Mark where platelets are.
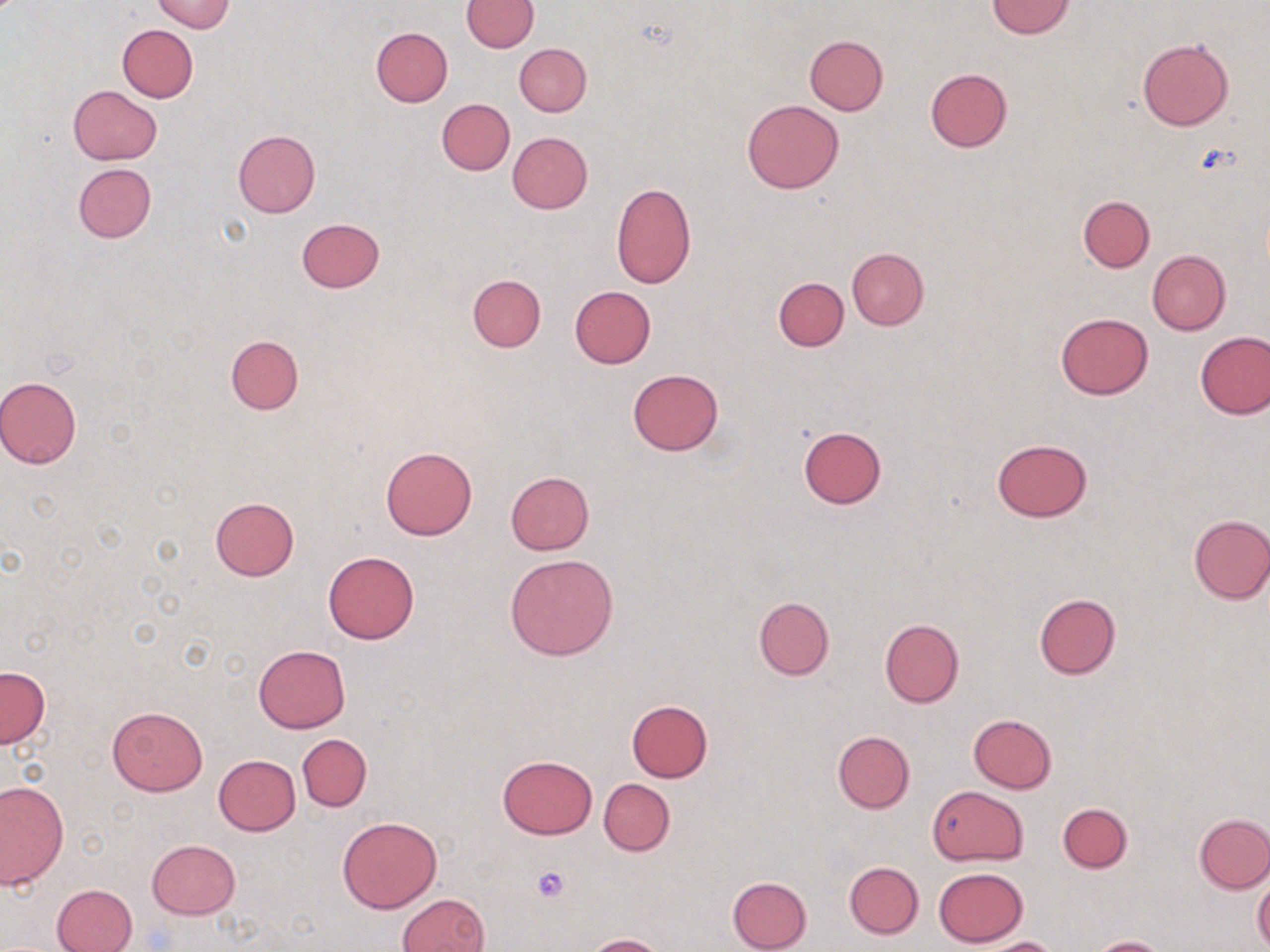

Approximate bounding boxes as named x1/y1/x2/y2 corners in pixels.
Platelets: (x1=532, y1=866, x2=569, y2=902).

Uninfected red blood cell locations: (x1=149, y1=0, x2=235, y2=33), (x1=462, y1=0, x2=537, y2=52), (x1=986, y1=1, x2=1076, y2=39), (x1=117, y1=24, x2=197, y2=102), (x1=370, y1=27, x2=452, y2=107), (x1=803, y1=35, x2=888, y2=115), (x1=1137, y1=38, x2=1234, y2=131), (x1=514, y1=42, x2=591, y2=116), (x1=925, y1=68, x2=1013, y2=152), (x1=69, y1=85, x2=162, y2=164), (x1=436, y1=99, x2=515, y2=175), (x1=741, y1=99, x2=844, y2=194), (x1=232, y1=129, x2=319, y2=218), (x1=507, y1=132, x2=593, y2=214), (x1=73, y1=163, x2=156, y2=243), (x1=611, y1=180, x2=696, y2=289), (x1=1078, y1=195, x2=1155, y2=272), (x1=296, y1=218, x2=385, y2=292), (x1=846, y1=248, x2=928, y2=330), (x1=1148, y1=250, x2=1230, y2=335), (x1=467, y1=274, x2=545, y2=351), (x1=774, y1=277, x2=849, y2=350), (x1=569, y1=286, x2=656, y2=368), (x1=1055, y1=311, x2=1154, y2=400), (x1=1195, y1=331, x2=1269, y2=419), (x1=225, y1=334, x2=304, y2=415), (x1=627, y1=368, x2=724, y2=455), (x1=0, y1=375, x2=81, y2=469), (x1=796, y1=427, x2=887, y2=509), (x1=991, y1=438, x2=1094, y2=523), (x1=381, y1=446, x2=477, y2=540), (x1=506, y1=471, x2=594, y2=554), (x1=210, y1=497, x2=300, y2=580), (x1=1186, y1=514, x2=1270, y2=604), (x1=323, y1=551, x2=418, y2=644), (x1=505, y1=553, x2=618, y2=661), (x1=1033, y1=593, x2=1121, y2=680), (x1=754, y1=596, x2=835, y2=681), (x1=880, y1=619, x2=964, y2=708), (x1=253, y1=645, x2=351, y2=733), (x1=0, y1=666, x2=50, y2=748), (x1=626, y1=700, x2=713, y2=782), (x1=106, y1=705, x2=208, y2=796), (x1=967, y1=714, x2=1057, y2=793), (x1=832, y1=731, x2=915, y2=814), (x1=297, y1=734, x2=371, y2=810), (x1=497, y1=754, x2=597, y2=839), (x1=214, y1=755, x2=299, y2=836), (x1=599, y1=778, x2=675, y2=856), (x1=0, y1=781, x2=67, y2=889), (x1=927, y1=786, x2=1027, y2=865), (x1=1058, y1=802, x2=1132, y2=873), (x1=1194, y1=813, x2=1270, y2=893), (x1=336, y1=815, x2=442, y2=914), (x1=147, y1=840, x2=240, y2=919), (x1=844, y1=861, x2=924, y2=938), (x1=933, y1=867, x2=1030, y2=947), (x1=1253, y1=874, x2=1270, y2=949), (x1=727, y1=875, x2=812, y2=952), (x1=52, y1=882, x2=138, y2=952), (x1=397, y1=893, x2=489, y2=952), (x1=585, y1=933, x2=668, y2=952), (x1=980, y1=936, x2=1061, y2=952), (x1=1089, y1=936, x2=1171, y2=952). Slide-level diagnosis: negative for blood parasites. May-Grünwald-Giemsa-stained preparation. Image is 1270×952 pixels. Single field of view. Thin blood film. Light microscopy. Captured at 1000x magnification.